Describe the morphology of the red blood cells.
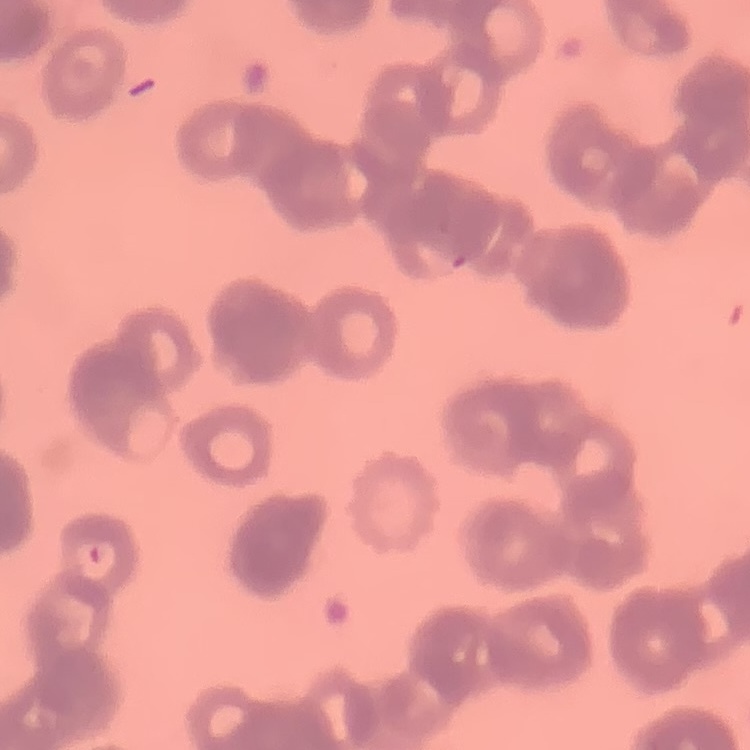

Rouleaux formation.

image type = one tile cut from a larger photomicrograph
preparation = thin blood smear
stain = Field's or Giemsa